Describe the morphology of the erythrocytes.
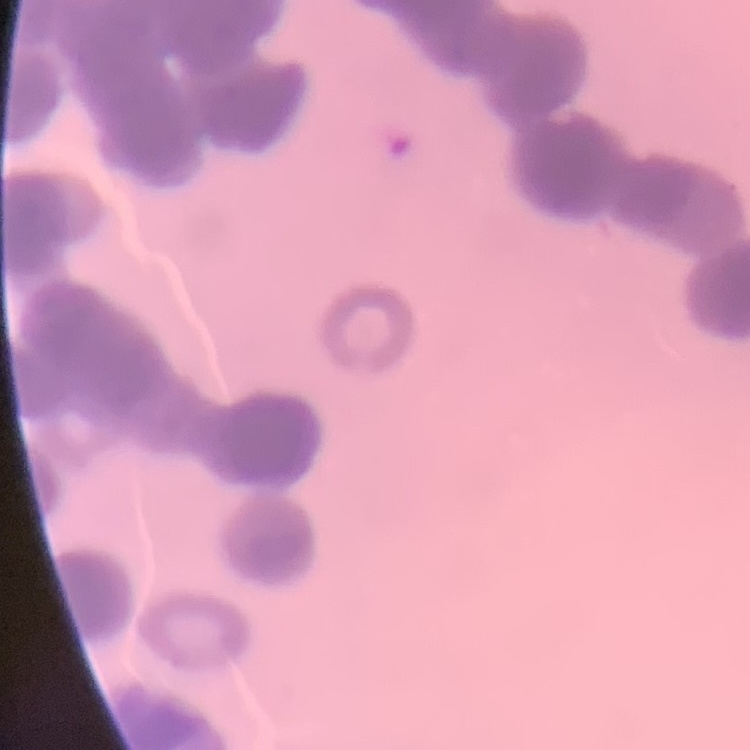
Rouleaux formation.

Square crop of a larger photomicrograph. Thin blood film. Field's or Giemsa stain.